Evaluate for malaria.
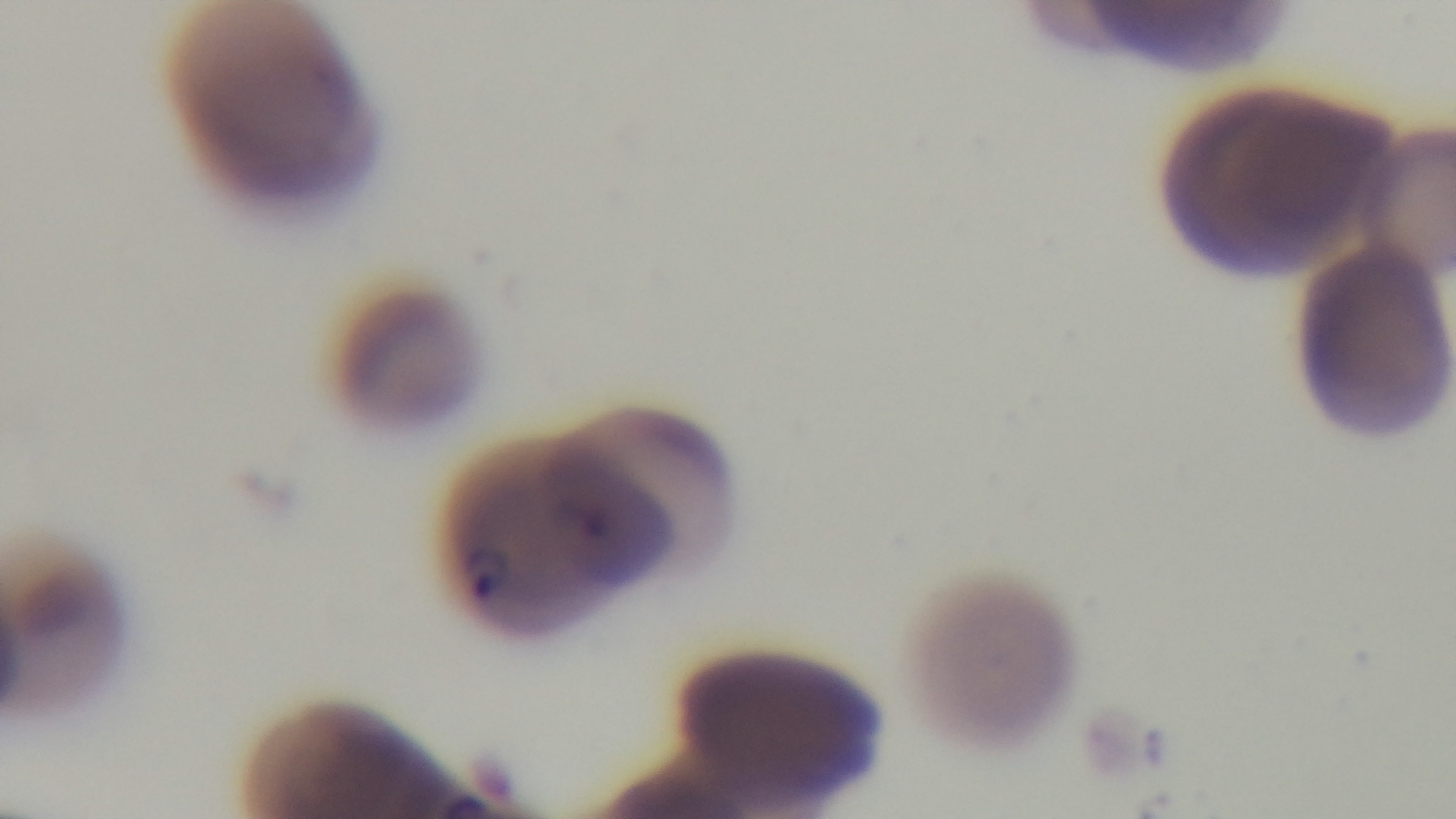

It is infected.

Summary:
  - Stain: Giemsa
  - Modality: light microscopy
  - Preparation: thin
  - Field of view: single
  - Capture: mounted 4K digital camera
  - Objective: 100x oil immersion